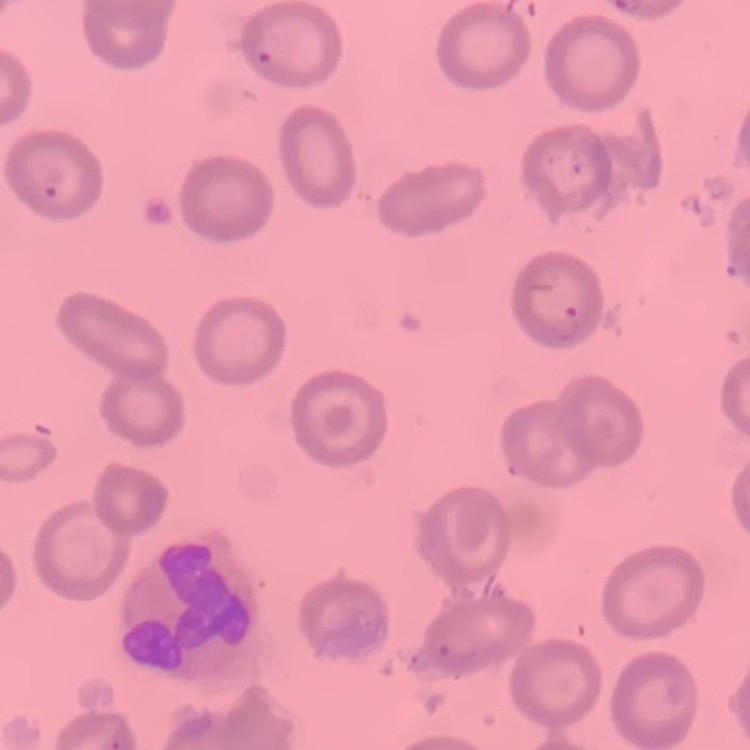
erythrocyte morphology = no rouleaux formation
stain = Field's or Giemsa
preparation = thin blood film
image type = one tile cut from a larger photomicrograph